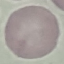 Result: no malaria parasites detected. Photographed with a smartphone camera at the microscope eyepiece. Thin blood film. Giemsa-stained preparation. Automatically extracted cell patch, resized to 64 × 64 pixels.